Report the malaria status of this cell.
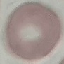

It is uninfected.

Summary:
  - Capture: smartphone through the microscope eyepiece
  - Stain: Giemsa
  - Preparation: thin blood smear
  - Image type: cell patch, automatically extracted from a larger field of view and resized to 64 × 64 pixels